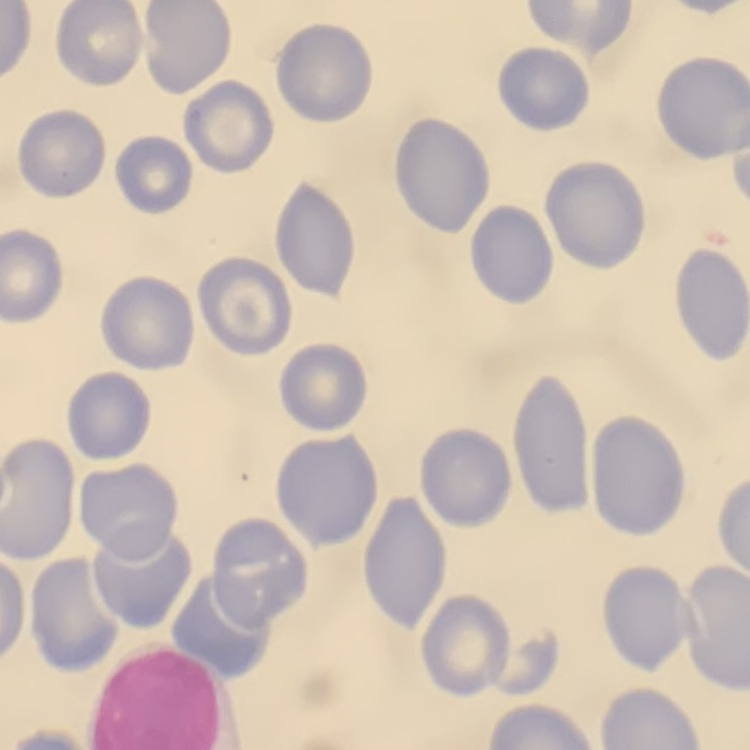

red blood cell morphology = no rouleaux formation
preparation = thin blood smear
image type = square crop of a larger photomicrograph
stain = Field's or Giemsa